Assess the morphology of the erythrocytes.
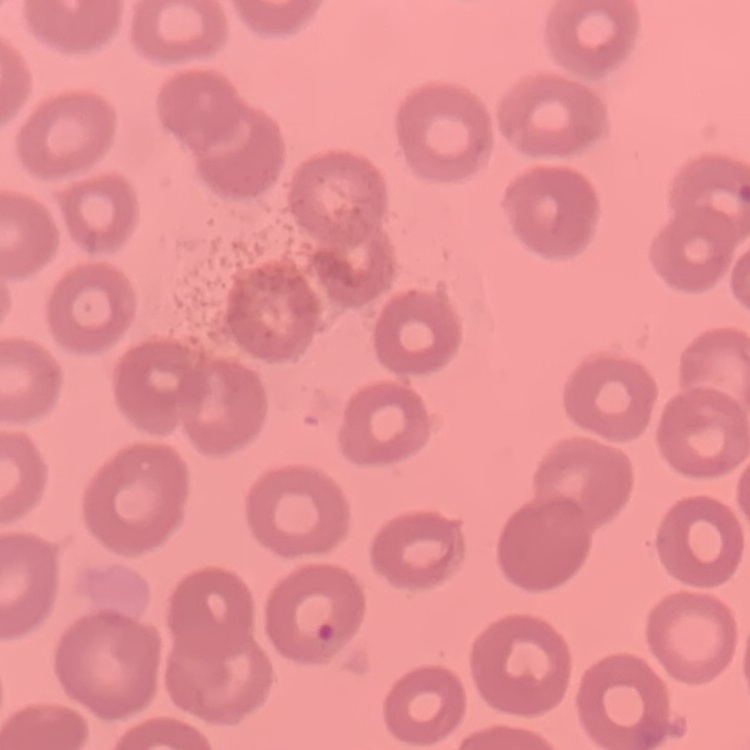
No rouleaux formation.

Summary:
  - Stain: Field's or Giemsa
  - Preparation: thin blood film
  - Image type: one tile cut from a larger photomicrograph